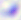 Photomicrograph. Toxoplasma gondii is seen. 400x magnification.